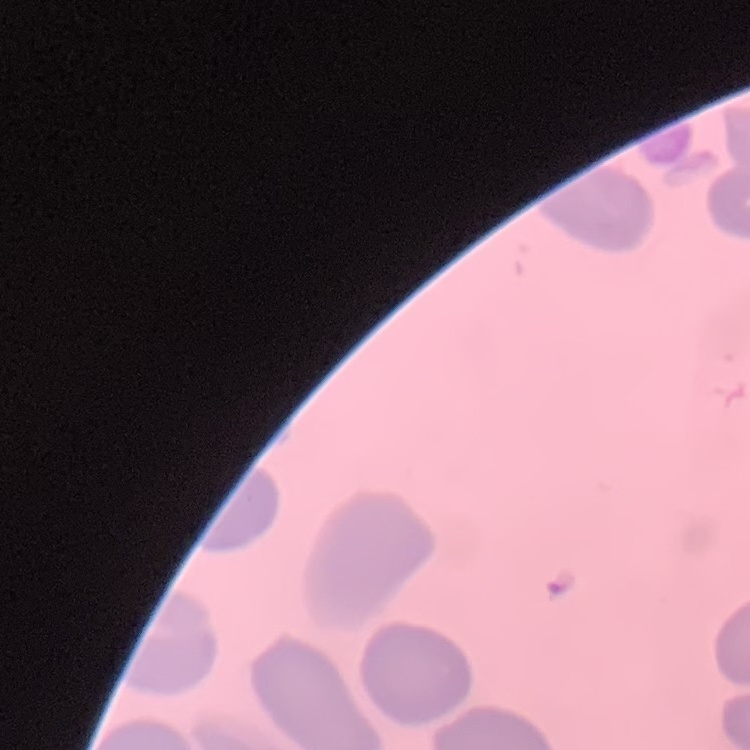

The red blood cells exhibit no rouleaux formation. Thin peripheral smear. Square crop of a larger photomicrograph. Stained with either Field's or Giemsa.